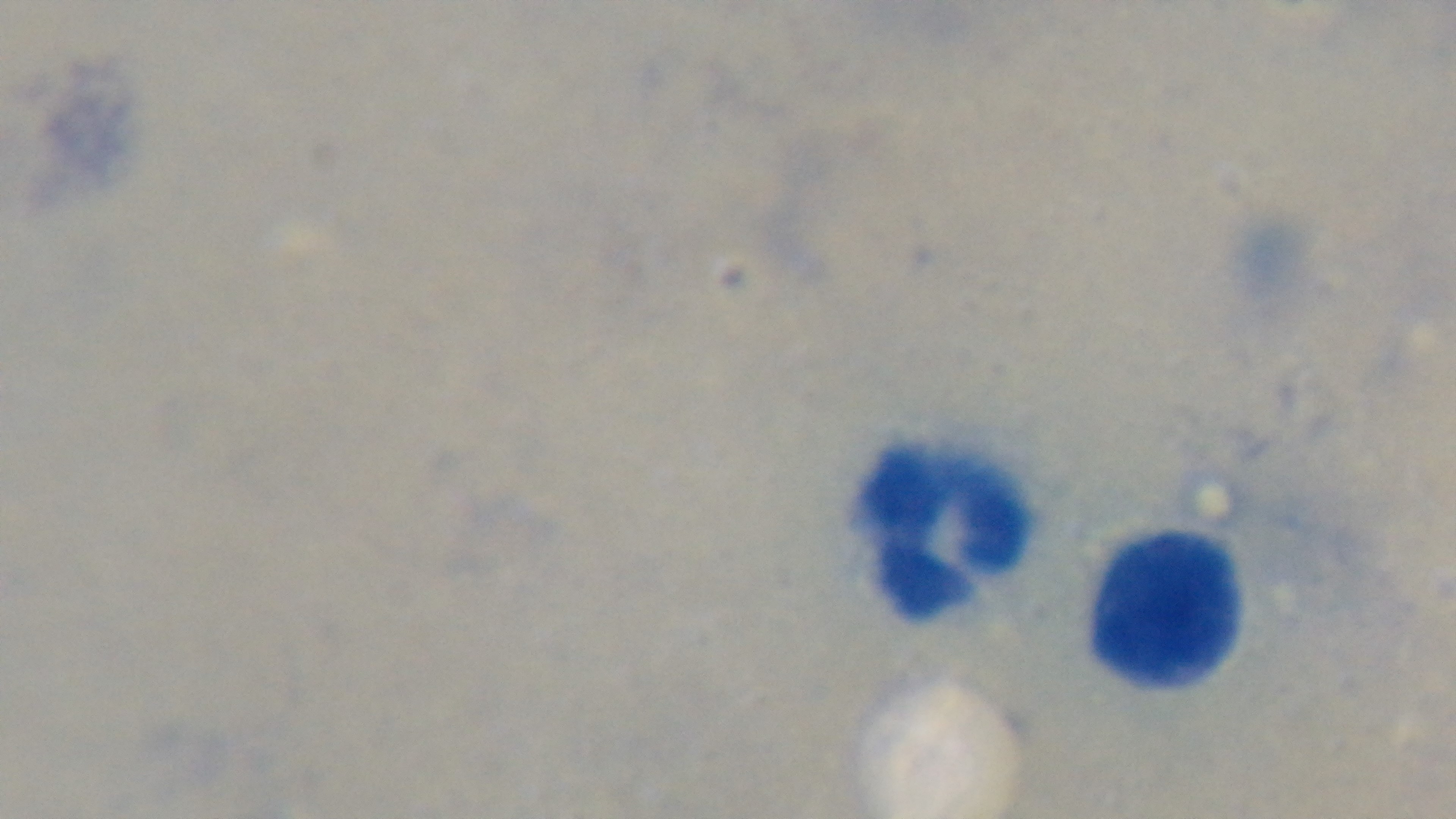

preparation = thick blood film
objective = 100x oil immersion
modality = light microscopy
capture = mounted 4K digital camera
malaria status = negative
field of view = single
stain = Giemsa